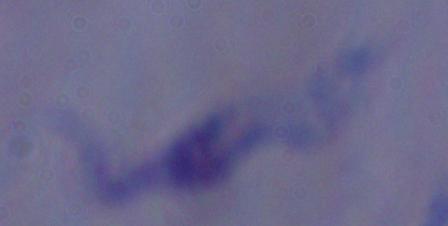

Summary:
  - Identification: trypanosome
  - Modality: micrograph
  - Magnification: 1000x